Locate every Plasmodium parasite.
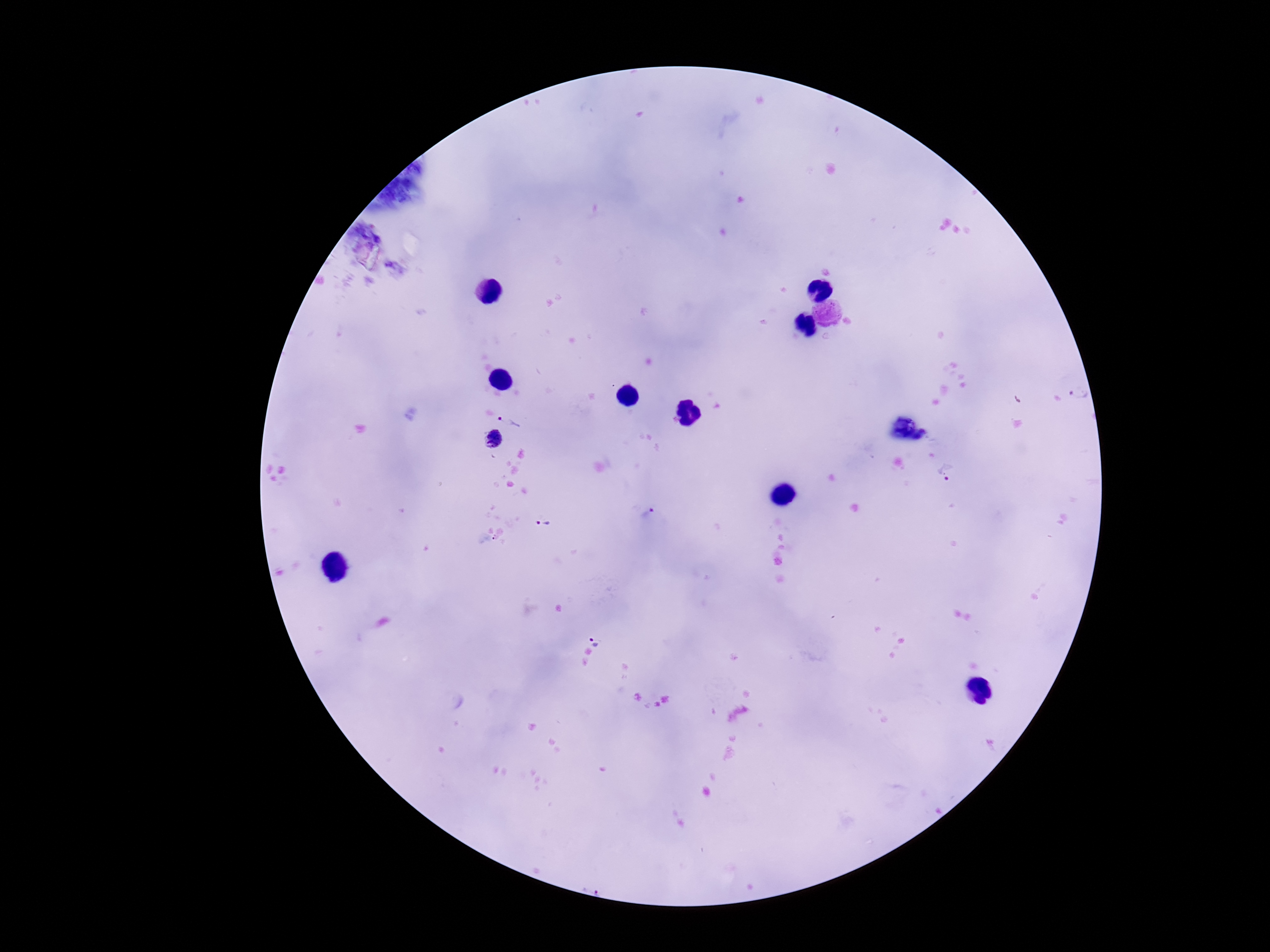

Approximate centers as (x, y) in pixels.
Plasmodium parasites: (1082, 395), (510, 421), (494, 439), (952, 473), (645, 512), (545, 525), (595, 639).

Summary:
  - Preparation: thick peripheral-blood smear
  - Field of view: one from this slide
  - Capture: smartphone camera through the microscope eyepiece
  - Stain: Giemsa
  - Image size: 1270×952 pixels
  - Magnification: 100x
  - Patient malaria status: infected